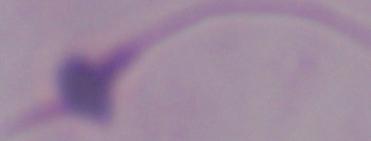 A Leishmania parasite is shown. 1000x magnification. Micrograph.